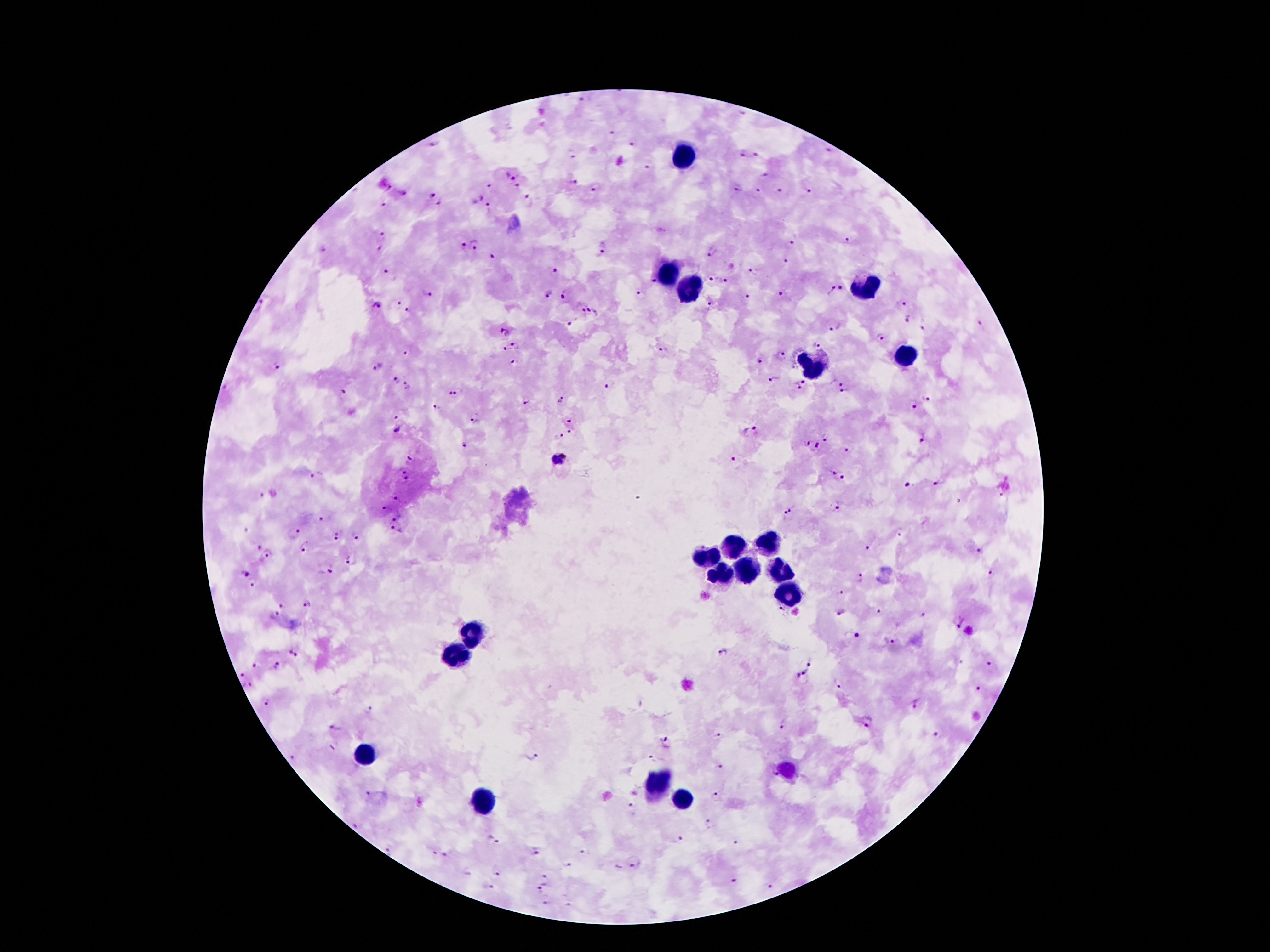

Approximate object centers, in pixels from the top-left corner.
Summary:
  - Leukocyte locations: (x=685, y=154), (x=665, y=269), (x=861, y=287), (x=686, y=290), (x=900, y=353), (x=818, y=366), (x=769, y=542), (x=737, y=546), (x=706, y=556), (x=744, y=567), (x=783, y=572), (x=720, y=574), (x=789, y=591), (x=471, y=633), (x=457, y=654), (x=364, y=751), (x=784, y=770), (x=655, y=784), (x=483, y=798), (x=681, y=798)
  - Plasmodium parasite locations: (x=583, y=99), (x=611, y=133), (x=435, y=144), (x=633, y=145), (x=829, y=149), (x=756, y=153), (x=742, y=154), (x=648, y=168), (x=511, y=174), (x=766, y=175), (x=572, y=182), (x=490, y=185), (x=518, y=185), (x=389, y=188), (x=595, y=190), (x=739, y=190), (x=759, y=192), (x=779, y=192), (x=809, y=193), (x=430, y=195), (x=478, y=198), (x=528, y=198), (x=382, y=204), (x=437, y=204), (x=490, y=210), (x=382, y=235), (x=848, y=239), (x=477, y=243), (x=794, y=243), (x=604, y=247), (x=463, y=248), (x=380, y=249), (x=323, y=252), (x=711, y=252), (x=492, y=259), (x=787, y=263), (x=554, y=270), (x=754, y=272), (x=389, y=274), (x=714, y=277), (x=725, y=280), (x=653, y=281), (x=841, y=288), (x=829, y=290), (x=428, y=291), (x=639, y=292), (x=565, y=293), (x=782, y=295), (x=546, y=296), (x=748, y=299), (x=397, y=301), (x=903, y=302), (x=261, y=306), (x=374, y=306), (x=710, y=306), (x=407, y=310), (x=595, y=311), (x=581, y=312), (x=907, y=319), (x=572, y=322), (x=981, y=324), (x=834, y=326), (x=923, y=329), (x=505, y=333), (x=880, y=337), (x=817, y=344), (x=515, y=346), (x=504, y=350), (x=664, y=351), (x=406, y=352), (x=781, y=355), (x=760, y=360), (x=513, y=364), (x=274, y=367), (x=378, y=367), (x=773, y=380), (x=395, y=382), (x=842, y=382), (x=803, y=383), (x=610, y=384), (x=408, y=385), (x=795, y=387), (x=346, y=392), (x=454, y=393), (x=842, y=394), (x=926, y=398), (x=528, y=400), (x=562, y=401), (x=439, y=407), (x=913, y=407), (x=396, y=418), (x=475, y=419), (x=570, y=419), (x=397, y=431), (x=750, y=432), (x=570, y=433), (x=560, y=436), (x=826, y=437), (x=922, y=438), (x=465, y=444), (x=806, y=444), (x=818, y=447), (x=848, y=451), (x=559, y=459), (x=411, y=460), (x=734, y=460), (x=400, y=470), (x=830, y=471), (x=316, y=475), (x=408, y=478), (x=844, y=479), (x=938, y=483), (x=908, y=487), (x=395, y=499), (x=835, y=506), (x=386, y=508), (x=786, y=511), (x=322, y=518), (x=395, y=518), (x=395, y=530), (x=295, y=531), (x=901, y=531), (x=335, y=533), (x=356, y=535), (x=256, y=547), (x=305, y=549), (x=867, y=549), (x=982, y=551), (x=269, y=553), (x=350, y=560), (x=331, y=572), (x=243, y=573), (x=994, y=573), (x=862, y=577), (x=252, y=585), (x=838, y=592), (x=308, y=605), (x=283, y=606), (x=779, y=609), (x=841, y=610), (x=879, y=610), (x=275, y=612), (x=923, y=615), (x=958, y=621), (x=857, y=635), (x=892, y=641), (x=295, y=651), (x=722, y=654), (x=809, y=662), (x=989, y=664), (x=257, y=666), (x=277, y=666), (x=803, y=673), (x=241, y=674), (x=839, y=683), (x=248, y=684), (x=980, y=689), (x=267, y=703), (x=914, y=705), (x=370, y=709), (x=868, y=723), (x=781, y=727), (x=334, y=729), (x=718, y=734), (x=936, y=735), (x=666, y=742), (x=532, y=756), (x=292, y=757), (x=652, y=757), (x=718, y=767), (x=369, y=794), (x=717, y=798), (x=630, y=807), (x=358, y=820), (x=708, y=824), (x=681, y=838), (x=492, y=839), (x=735, y=842), (x=535, y=851), (x=389, y=852), (x=584, y=852), (x=435, y=853), (x=447, y=855), (x=634, y=860), (x=569, y=864), (x=497, y=871), (x=548, y=878), (x=735, y=881), (x=489, y=885), (x=541, y=887), (x=547, y=903), (x=568, y=905)
  - Stain: Giemsa
  - Preparation: thick peripheral-blood smear
  - Field of view: one from this slide
  - Image size: 1270×952 pixels
  - Capture: smartphone through the microscope eyepiece
  - Patient malaria status: infected with Plasmodium falciparum
  - Magnification: 100x